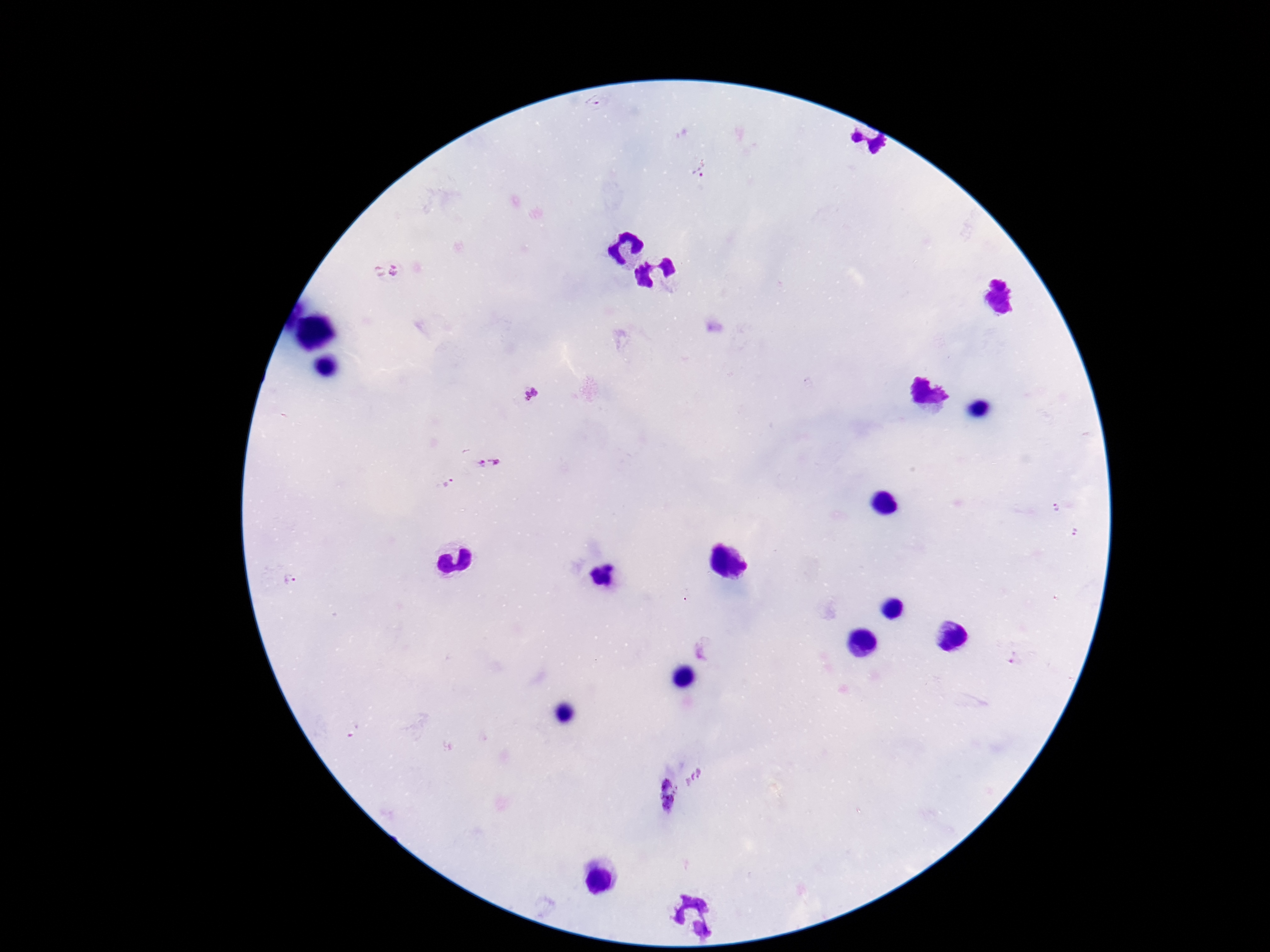
magnification: 100x
capture: smartphone camera through the microscope eyepiece
stain: Giemsa
image_size: 1270×952 pixels
preparation: thick peripheral-blood smear
field_of_view: one from this slide
patient_malaria_status: positive
plasmodium_parasite_locations: 'approximate centers as [x, y] in pixels: [594, 102], [701, 169], [386, 272], [533, 394], [491, 462], [449, 484], [1056, 507], [1075, 533], [293, 583], [1015, 657], [695, 777], [664, 796]'